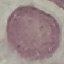 Malaria status: uninfected. Thin blood smear. Photographed with a smartphone camera at the microscope eyepiece. Giemsa-stained preparation. Cell patch, automatically extracted from a larger field of view and resized to 64 × 64 pixels.